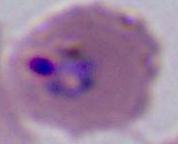 Captured at either 400x or 1000x magnification. Micrograph. A Plasmodium parasite is shown.